Outline each blood parasite and name the species.
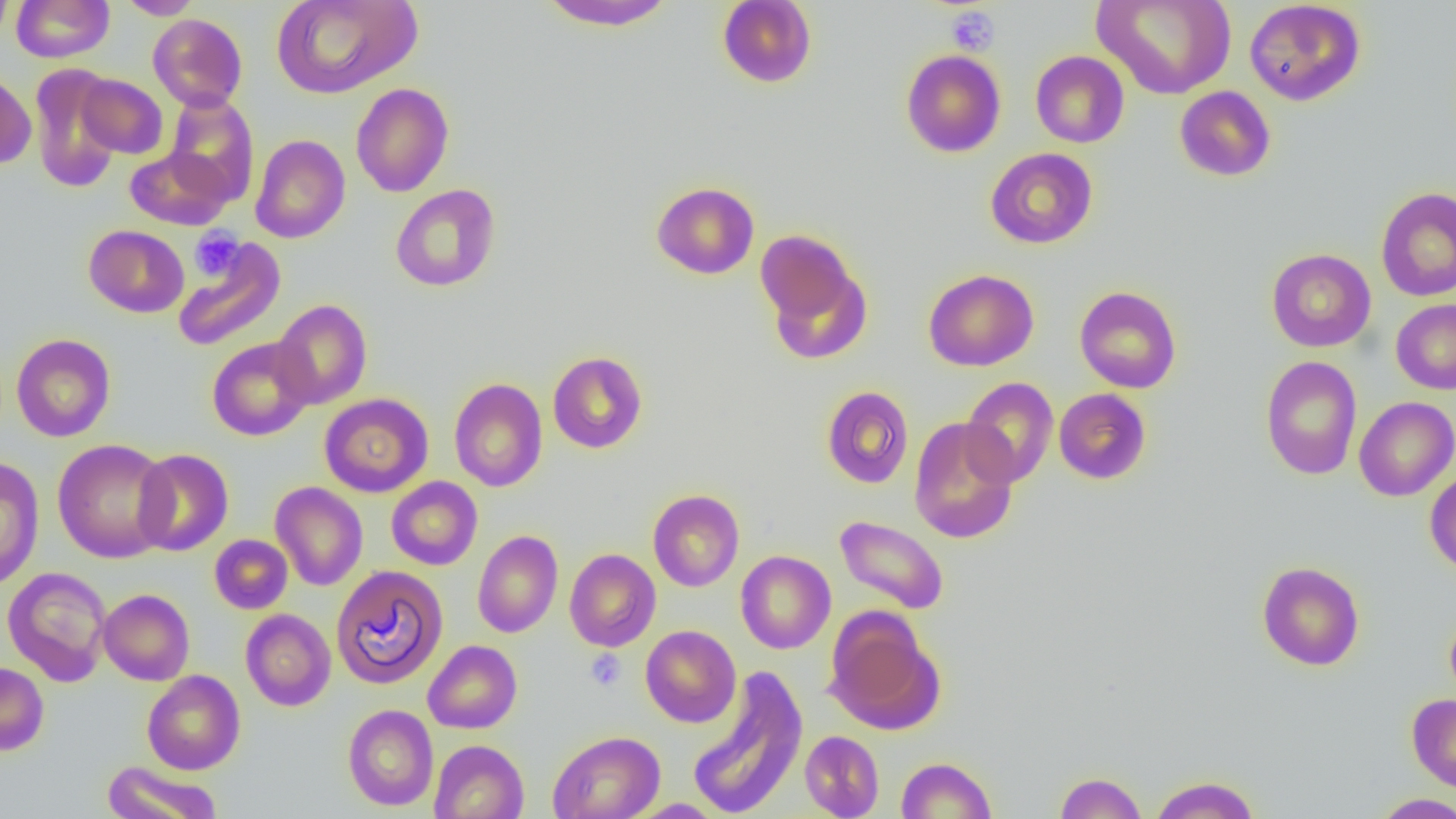

No blood parasites seen.

slide-level diagnosis = no evidence of blood parasites
image size = 1456×819 pixels
magnification = 1000x
modality = optical microscopy
platelet locations = approximate bounding boxes as [x1, y1, x2, y2] in pixels: [945, 7, 1000, 56], [189, 228, 244, 281], [585, 649, 626, 691]
field of view = single
preparation = thin blood film
uninfected red blood cell locations = approximate bounding boxes as [x1, y1, x2, y2] in pixels: [0, 0, 14, 45], [11, 0, 114, 62], [117, 0, 203, 19], [271, 0, 421, 99], [536, 0, 680, 31], [1094, 0, 1236, 99], [1244, 0, 1366, 106], [716, 1, 817, 88], [148, 14, 248, 111], [901, 49, 1006, 157], [1030, 50, 1130, 148], [28, 64, 124, 193], [0, 69, 36, 170], [76, 74, 168, 159], [350, 82, 454, 197], [1174, 86, 1276, 182], [163, 93, 259, 204], [250, 134, 350, 243], [125, 147, 232, 230], [985, 147, 1098, 249], [650, 181, 760, 280], [390, 184, 501, 292], [1375, 187, 1456, 301], [84, 225, 190, 318], [756, 230, 866, 353], [172, 239, 286, 351], [1266, 248, 1376, 352], [923, 268, 1039, 371], [1074, 286, 1182, 393], [271, 299, 372, 409], [1391, 299, 1456, 394], [11, 333, 115, 442], [207, 337, 316, 441], [547, 351, 647, 454], [1260, 356, 1362, 480], [448, 377, 548, 492], [961, 377, 1058, 487], [821, 385, 914, 489], [1054, 388, 1152, 484], [319, 393, 433, 498], [1354, 396, 1456, 501], [908, 417, 1020, 544], [52, 438, 174, 563], [132, 449, 234, 555], [0, 456, 44, 591], [1425, 469, 1456, 575], [386, 476, 482, 570], [270, 482, 368, 591], [647, 489, 744, 592], [834, 515, 949, 614], [473, 530, 563, 638], [209, 534, 292, 614], [564, 548, 661, 651], [735, 550, 835, 654], [1256, 561, 1365, 671], [331, 565, 449, 689], [3, 567, 112, 686], [99, 589, 194, 685], [241, 609, 336, 711], [825, 609, 944, 734], [1445, 609, 1456, 706], [641, 625, 741, 727], [423, 640, 522, 734], [0, 661, 49, 756], [688, 666, 808, 818], [142, 670, 245, 775], [1407, 693, 1456, 793], [342, 704, 439, 811], [548, 730, 665, 819], [800, 730, 884, 818], [429, 739, 529, 819], [896, 756, 997, 818], [102, 760, 222, 819], [1054, 771, 1147, 818], [1150, 774, 1261, 818], [1372, 793, 1456, 818], [626, 799, 725, 818]